Assess for malaria.
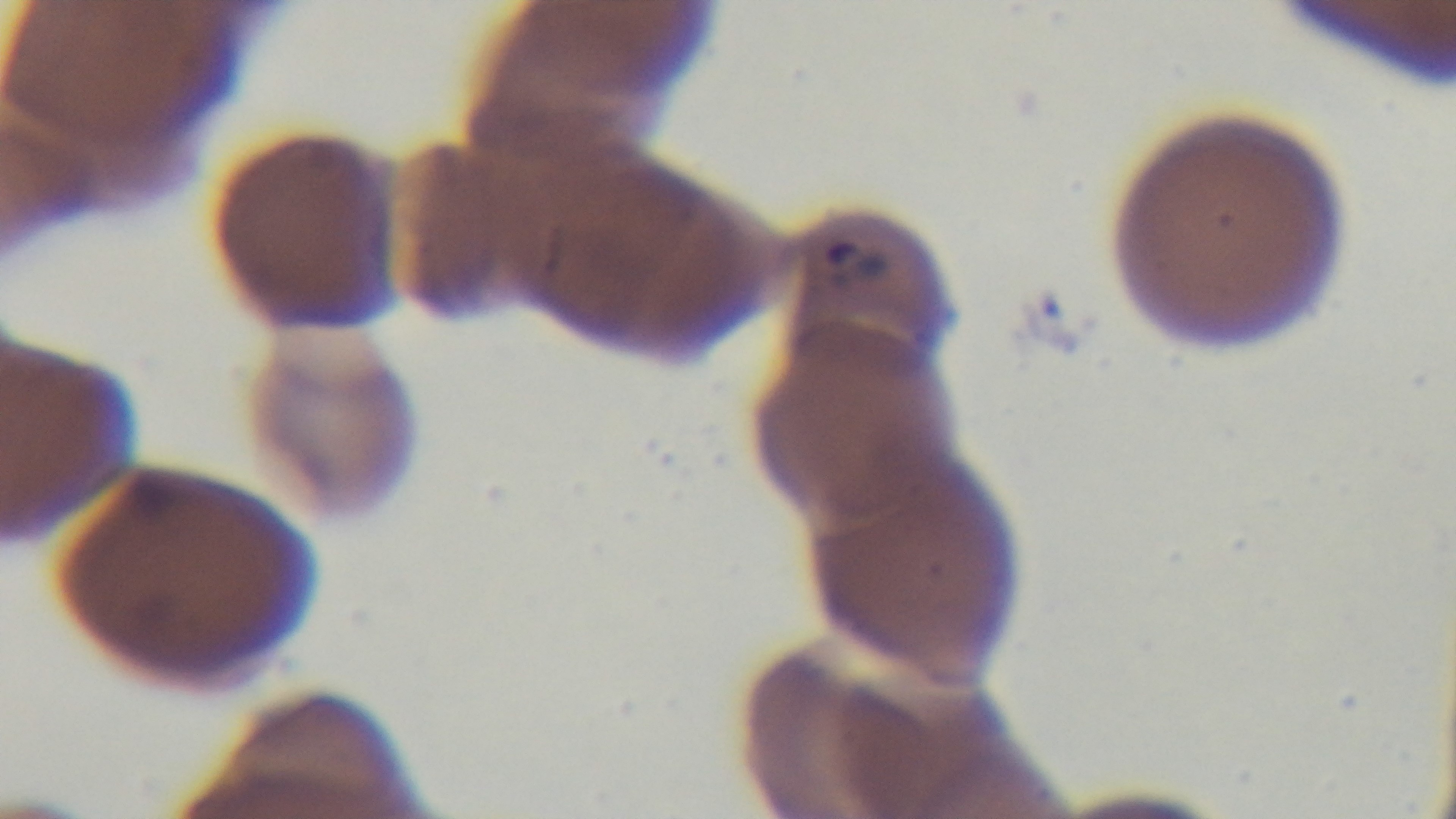

It is infected.

One field from the slide. Giemsa-stained. Oil-immersion objective, 100x. Light microscopy. Preparation: thin. Captured with a mounted 4K digital camera.